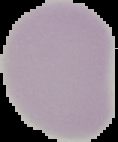
Summary:
  - Image size: 118×142 pixels
  - Image type: segmented cell region on a black background
  - Preparation: thin blood smear
  - Malaria status: uninfected